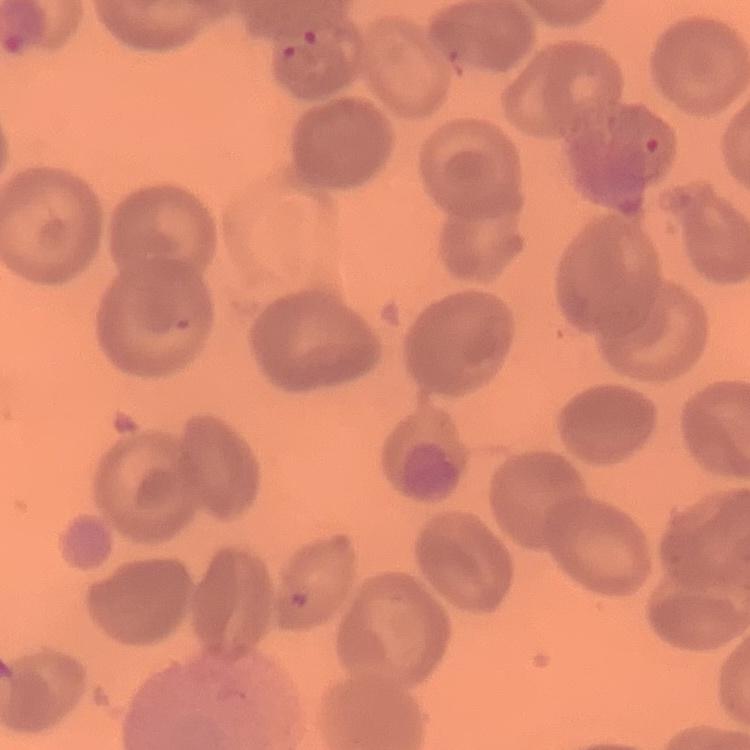

The erythrocytes show no rouleaux formation. Field's or Giemsa stain. Thin blood film. Square crop of a larger photomicrograph.